Outline each blood parasite and name the species.
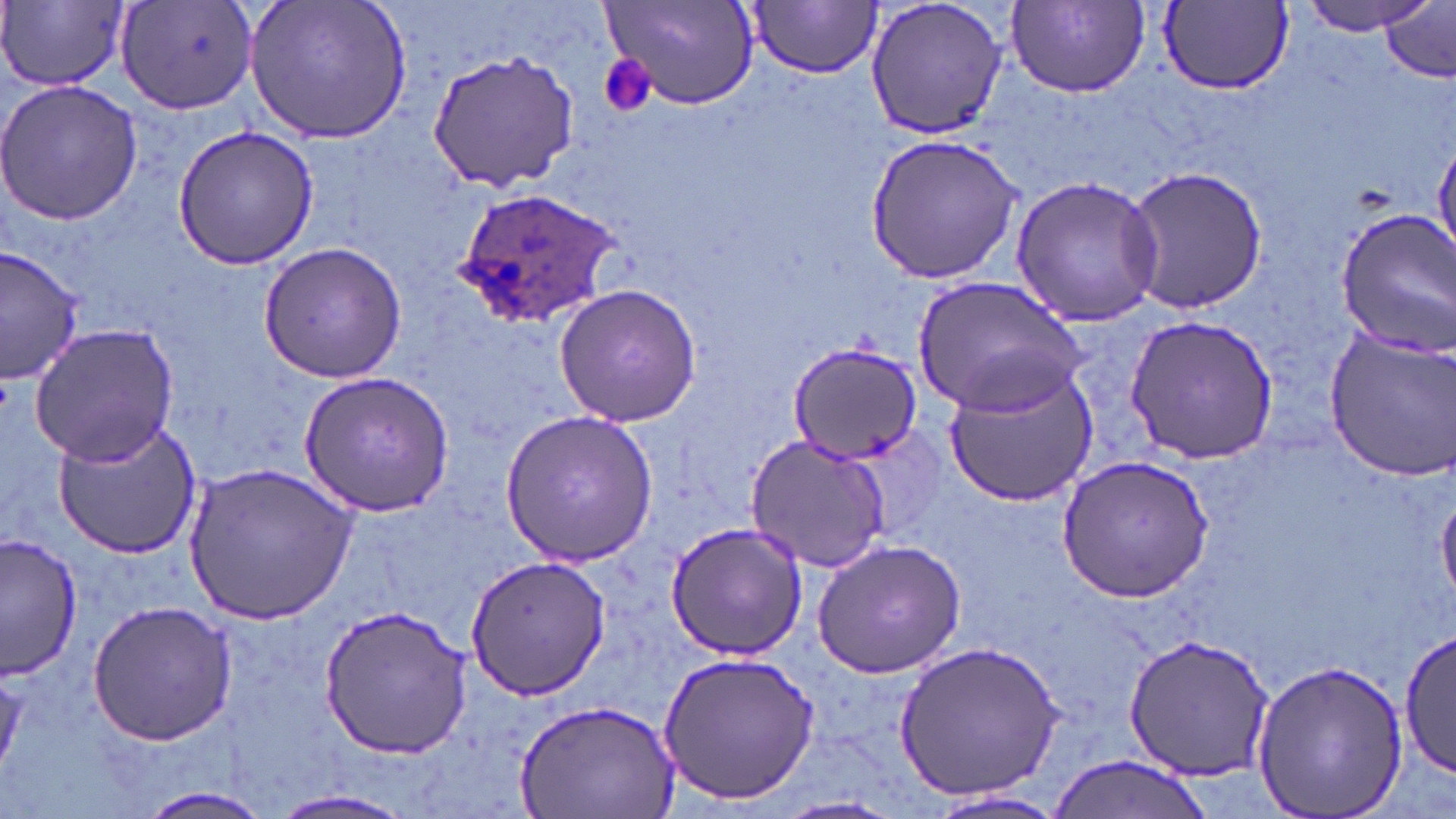

Approximate bounding boxes as (x1, y1, x2, y2) in pixels.
Plasmodium ovale-infected red blood cells: (450, 188, 625, 328).
No Plasmodium falciparum, Plasmodium malariae, Plasmodium vivax, Babesia divergens, or Trypanosoma brucei observed.

Platelet locations: (599, 55, 656, 119). Uninfected red blood cell locations: (245, 0, 412, 146), (864, 0, 1009, 141), (1298, 0, 1436, 34), (117, 1, 258, 115), (747, 2, 882, 78), (1007, 2, 1151, 96), (1159, 2, 1294, 93), (0, 3, 128, 92), (599, 3, 760, 111), (1378, 4, 1455, 80), (425, 49, 578, 194), (0, 79, 144, 223), (170, 124, 321, 271), (863, 132, 1026, 286), (1124, 167, 1268, 313), (1009, 176, 1165, 328), (1331, 210, 1456, 358), (257, 240, 409, 384), (1, 244, 85, 383), (913, 276, 1085, 415), (553, 285, 701, 429), (1123, 313, 1279, 465), (29, 322, 180, 468), (1322, 328, 1456, 481), (788, 339, 925, 462), (940, 361, 1100, 509), (302, 370, 455, 512), (498, 410, 656, 567), (49, 420, 202, 559), (744, 432, 895, 573), (1055, 455, 1213, 601), (185, 460, 359, 625), (1437, 487, 1456, 602), (665, 522, 808, 660), (2, 533, 82, 677), (812, 539, 966, 677), (463, 555, 613, 701), (88, 601, 236, 744), (316, 601, 473, 759), (1401, 627, 1455, 776), (1120, 633, 1273, 783), (892, 638, 1066, 806), (659, 650, 820, 804), (1248, 658, 1409, 819), (517, 698, 679, 819), (1046, 755, 1218, 819), (132, 784, 275, 818), (269, 789, 420, 819), (923, 789, 1072, 819), (774, 795, 904, 818). Slide-level diagnosis: Plasmodium ovale. Captured at 1000x magnification. Thin blood film. Single field of view. Light microscopy. May-Grünwald-Giemsa stain. Image is 1456×819 pixels.